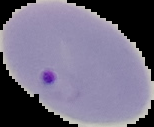 Image is 154×127 pixels. From a thin blood film. Result: malaria parasites identified. The area outside the segmented cell region is set to black.